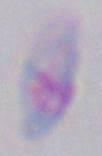

modality: photomicrograph
magnification: 1000x
identification: Toxoplasma gondii